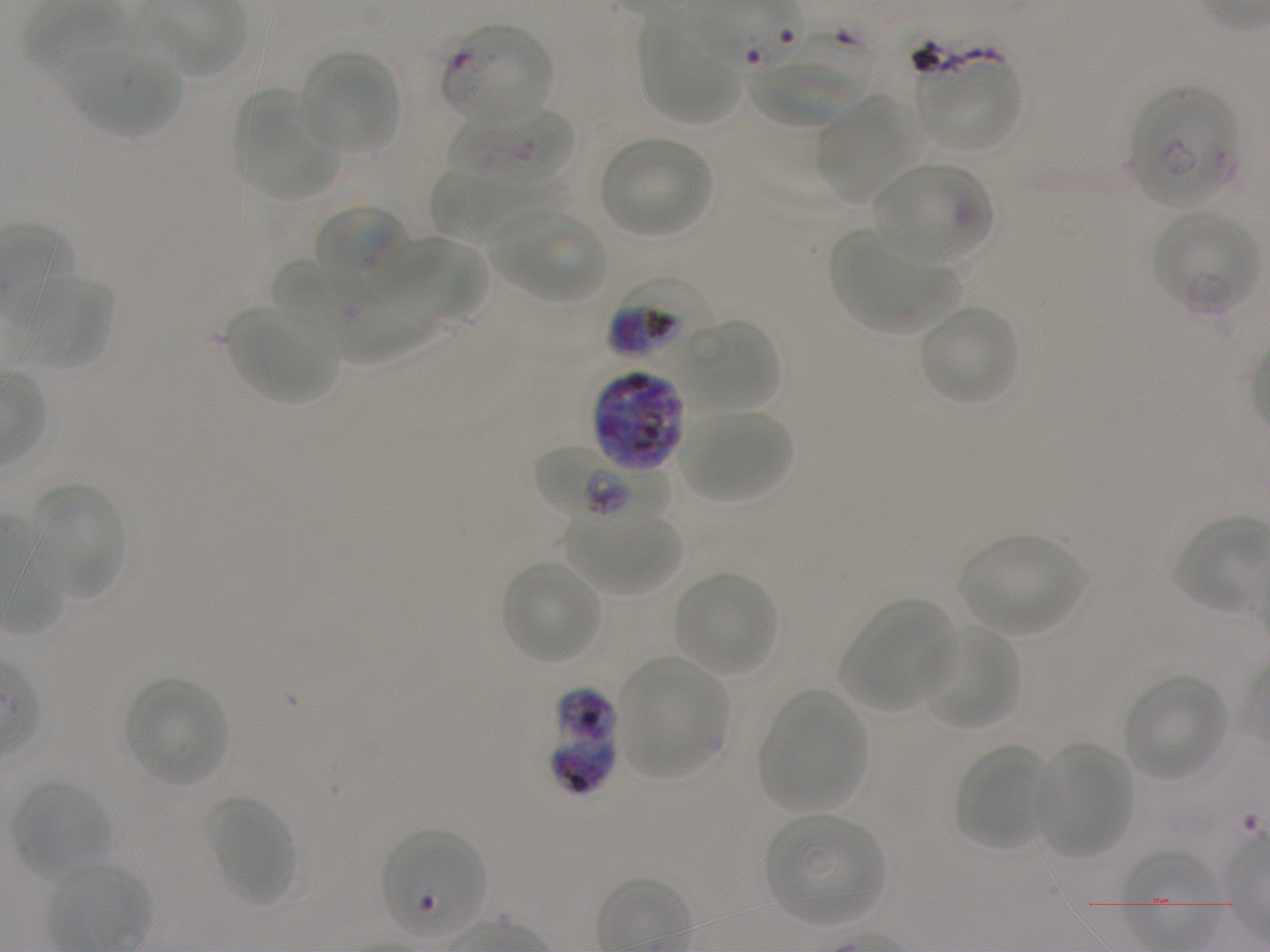 Approximate bounding boxes as [x1, y1, x2, y2] in pixels. Not every red blood cell is marked. A life-cycle stage — or a range of stages, where the recorded stages span more than one — follows each staged infected red blood cell. Locations of uninfected red blood cells: [641, 20, 742, 122], [58, 46, 182, 139], [297, 51, 401, 155], [919, 57, 1020, 153], [747, 58, 860, 127], [234, 90, 339, 201], [815, 96, 928, 201], [598, 135, 712, 238], [874, 163, 990, 263], [429, 166, 573, 242], [313, 204, 408, 283], [486, 210, 606, 301], [829, 230, 960, 332], [368, 237, 486, 327], [270, 258, 368, 331], [17, 275, 115, 369], [329, 282, 440, 367], [919, 303, 1019, 406], [228, 305, 339, 405], [682, 317, 783, 414], [681, 409, 795, 504], [29, 483, 125, 597], [564, 511, 682, 595], [958, 533, 1087, 636], [499, 559, 602, 666], [674, 572, 777, 676], [839, 599, 956, 712], [920, 624, 1020, 733], [617, 655, 727, 778], [1121, 674, 1228, 782], [124, 677, 231, 787], [759, 690, 867, 812], [954, 742, 1052, 852], [1032, 742, 1132, 859], [10, 780, 112, 876], [204, 794, 295, 905], [766, 813, 885, 926], [380, 829, 486, 939]. Locations of red blood cells of indeterminate infection status: [793, 28, 877, 103]. Locations of infected red blood cells: [441, 23, 552, 124]; [1132, 88, 1240, 209]; [449, 104, 575, 191] ring; [1151, 211, 1259, 315] late ring to early trophozoite; [608, 273, 714, 366] early trophozoite to early schizont; [590, 369, 687, 471]; [534, 447, 672, 518]; [549, 687, 619, 796]. Giemsa-stained preparation. Oil immersion, 100x objective (numerical aperture 1.25). Image is 1270×952 pixels. Thin blood smear. One field from this slide. Plasmodium falciparum strain NF54 in static in-vitro culture. Donor blood group A+.